Classify this cell by malaria status.
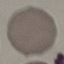
Uninfected.

Giemsa stain. Thin blood film. Cell patch, automatically extracted from a larger field of view and resized to 64 × 64 pixels. Acquired by smartphone through the microscope eyepiece.